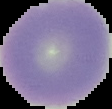
Segmented cell region on a black background. From a thin blood film. Result: negative for malaria parasites. Image is 112×109 pixels.